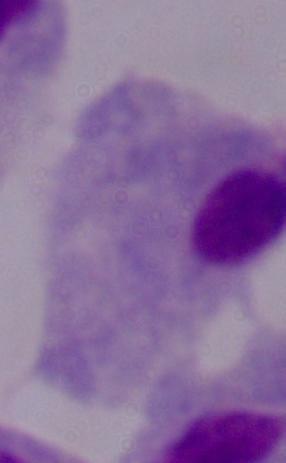

Summary:
  - Identification: trichomonad
  - Modality: micrograph
  - Magnification: 1000x